Name the blood parasite species.
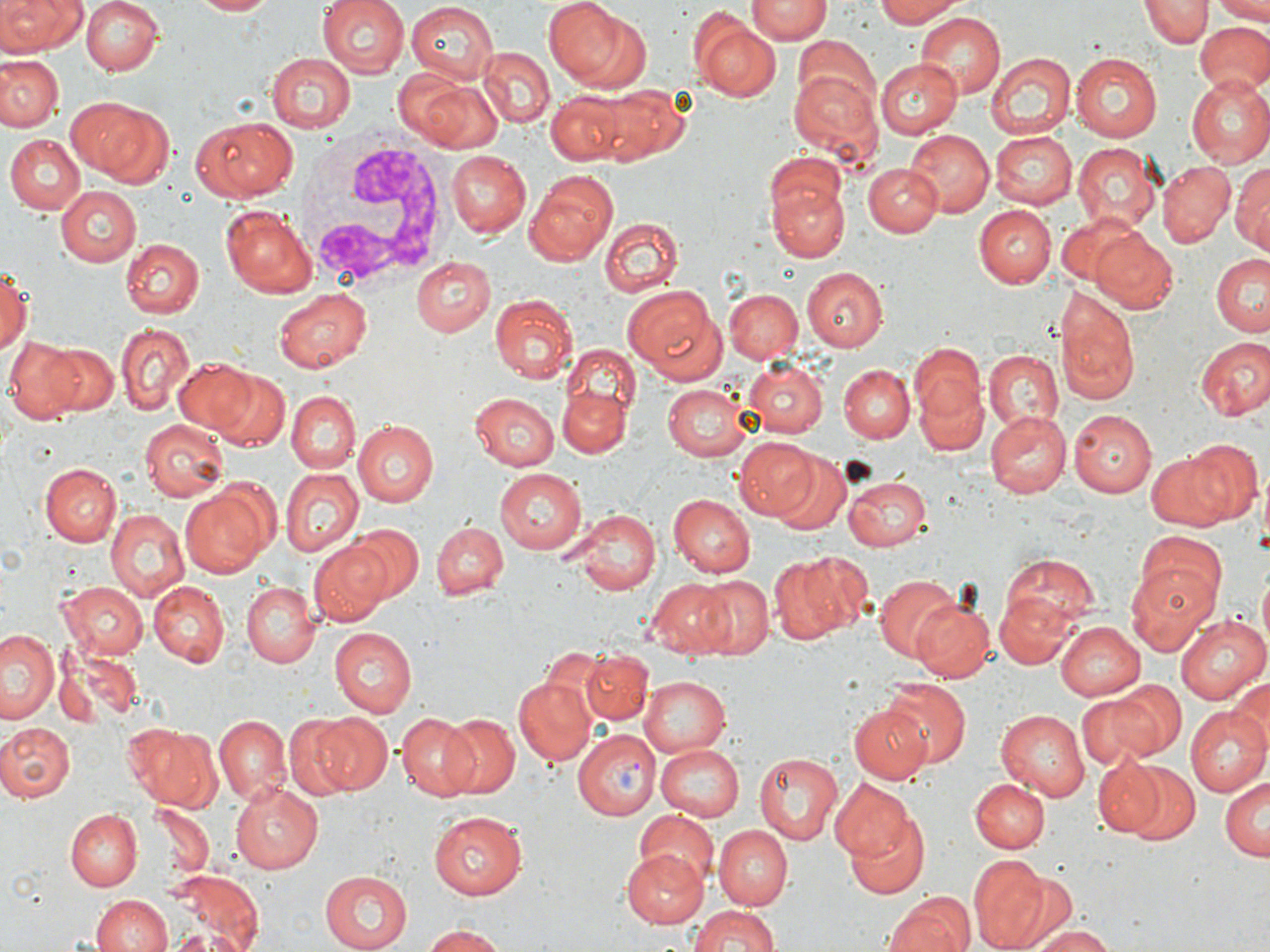

Plasmodium vivax.

preparation = thin blood smear
stain = May-Grünwald-Giemsa
uninfected red blood cell locations = approximate bounding boxes as (x1,y1)-(x2,y2) corner pairs in pixels: (0,0)-(84,56), (80,0)-(161,75), (191,0)-(277,16), (319,0)-(410,78), (544,0)-(632,85), (746,0)-(829,43), (872,0)-(967,28), (1143,0)-(1209,47), (1213,0)-(1270,22), (407,3)-(499,83), (915,13)-(1005,99), (693,18)-(780,102), (1193,21)-(1270,99), (791,34)-(878,118), (475,46)-(554,128), (265,51)-(354,132), (0,53)-(62,131), (1071,53)-(1163,140), (987,54)-(1075,141), (876,57)-(961,139), (787,69)-(882,166), (394,70)-(506,154), (1184,77)-(1270,165), (590,85)-(694,165), (545,93)-(633,166), (68,97)-(162,182), (190,117)-(300,202), (992,130)-(1079,209), (907,131)-(994,216), (986,132)-(1069,290), (5,134)-(83,213), (1071,143)-(1162,236), (445,151)-(531,237), (763,153)-(844,225), (1232,157)-(1269,250), (1156,158)-(1236,246), (864,162)-(944,235), (526,171)-(622,265), (771,183)-(847,262), (55,186)-(141,266), (975,204)-(1057,287), (219,205)-(316,298), (1055,212)-(1146,288), (599,218)-(683,297), (1089,229)-(1180,314), (120,238)-(204,319), (1212,251)-(1270,337), (409,255)-(495,336), (0,262)-(31,357), (811,265)-(901,428), (803,267)-(890,351), (623,283)-(723,380), (1054,287)-(1139,406), (273,289)-(371,371), (725,289)-(804,364), (490,293)-(577,383), (115,323)-(193,415), (1194,336)-(1269,420), (6,337)-(104,423), (909,343)-(987,435), (45,344)-(118,415), (559,344)-(639,430), (982,349)-(1065,434), (172,357)-(261,440), (742,359)-(828,437), (840,364)-(915,443), (202,366)-(291,453), (915,382)-(986,456), (662,383)-(753,462), (557,388)-(630,456), (285,392)-(360,473), (469,393)-(560,471), (1071,408)-(1159,497), (985,409)-(1071,497), (139,420)-(228,500), (354,421)-(438,505), (735,437)-(821,521), (1185,438)-(1264,526), (1145,449)-(1245,530), (774,455)-(852,536), (40,464)-(120,546), (496,468)-(587,553), (280,470)-(362,557), (844,472)-(930,552), (182,488)-(270,576), (668,495)-(755,578), (566,510)-(660,595), (105,512)-(189,602), (433,521)-(507,600), (347,523)-(422,602), (1134,532)-(1227,623), (310,541)-(393,625), (771,551)-(868,643), (998,555)-(1101,639), (1125,561)-(1221,656), (873,573)-(962,661), (694,577)-(772,657), (648,578)-(737,656), (150,581)-(230,665), (241,581)-(321,669), (57,582)-(149,659), (997,592)-(1077,669), (912,597)-(996,680), (1175,614)-(1266,704), (1054,618)-(1144,701), (2,627)-(61,724), (328,629)-(416,717), (52,642)-(142,724), (579,650)-(651,725), (1230,673)-(1270,761), (514,676)-(599,766), (640,676)-(732,757), (882,676)-(971,768), (1109,678)-(1187,759), (1079,691)-(1162,771), (849,705)-(929,784), (1184,707)-(1270,800), (996,708)-(1090,802), (395,711)-(480,801), (312,712)-(393,794), (283,713)-(358,800), (439,713)-(520,797), (215,716)-(289,803), (1,722)-(77,801), (124,724)-(222,811), (658,742)-(747,821), (754,751)-(844,845), (1091,756)-(1175,839), (1122,762)-(1201,847), (1219,776)-(1269,864), (968,777)-(1050,855), (830,779)-(913,861), (231,781)-(324,874), (153,806)-(214,877), (65,809)-(142,891), (839,809)-(932,898), (426,810)-(528,901), (634,813)-(718,890), (712,823)-(793,910), (623,849)-(709,929), (970,853)-(1050,951), (994,867)-(1083,952), (167,870)-(262,952), (316,870)-(410,952), (886,889)-(974,952), (91,895)-(174,952), (686,903)-(785,952), (1025,925)-(1119,952), (421,926)-(509,951)
white blood cell locations = approximate bounding boxes as (x1,y1)-(x2,y2) corner pairs in pixels: (294,133)-(454,296)
Plasmodium vivax-infected red blood cell locations = approximate bounding boxes as (x1,y1)-(x2,y2) corner pairs in pixels: (574,730)-(660,819)
magnification = 1000x
image size = 1270×952 pixels
modality = optical microscopy
field of view = one of a larger specimen